Give the position of every leukocyte visible.
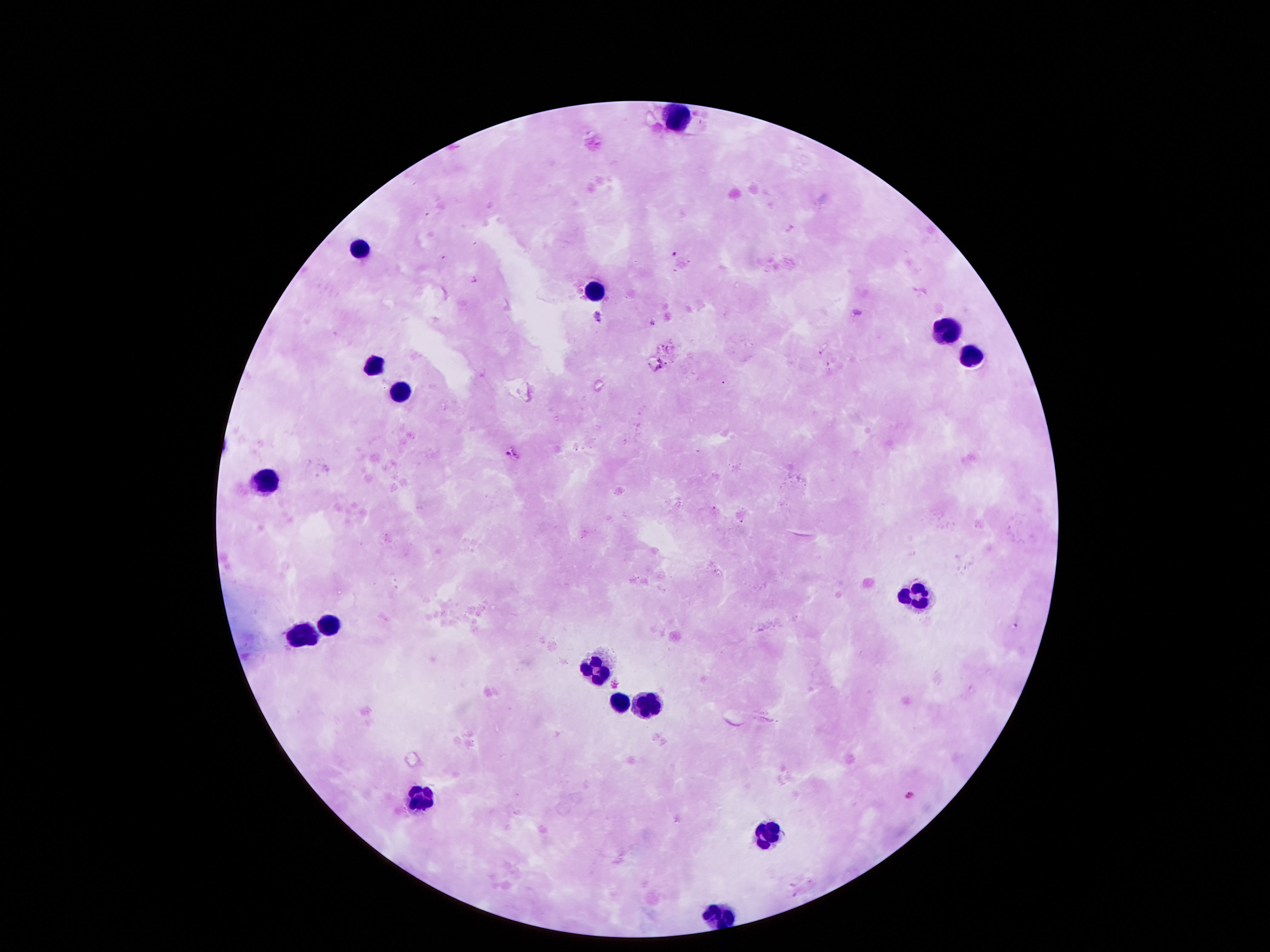

Approximate centers as [x, y] in pixels.
Leukocytes: [682, 114], [360, 248], [588, 286], [942, 325], [973, 358], [374, 365], [398, 391], [265, 479], [913, 597], [332, 615], [304, 636], [602, 663], [619, 699], [647, 702], [416, 803], [770, 831], [721, 910].

100x magnification. Single field of view. Image is 1270×952 pixels. Patient malaria status: negative. Photographed through the microscope eyepiece with a smartphone camera. Giemsa stain. Thick blood film.